Mark where platelets are.
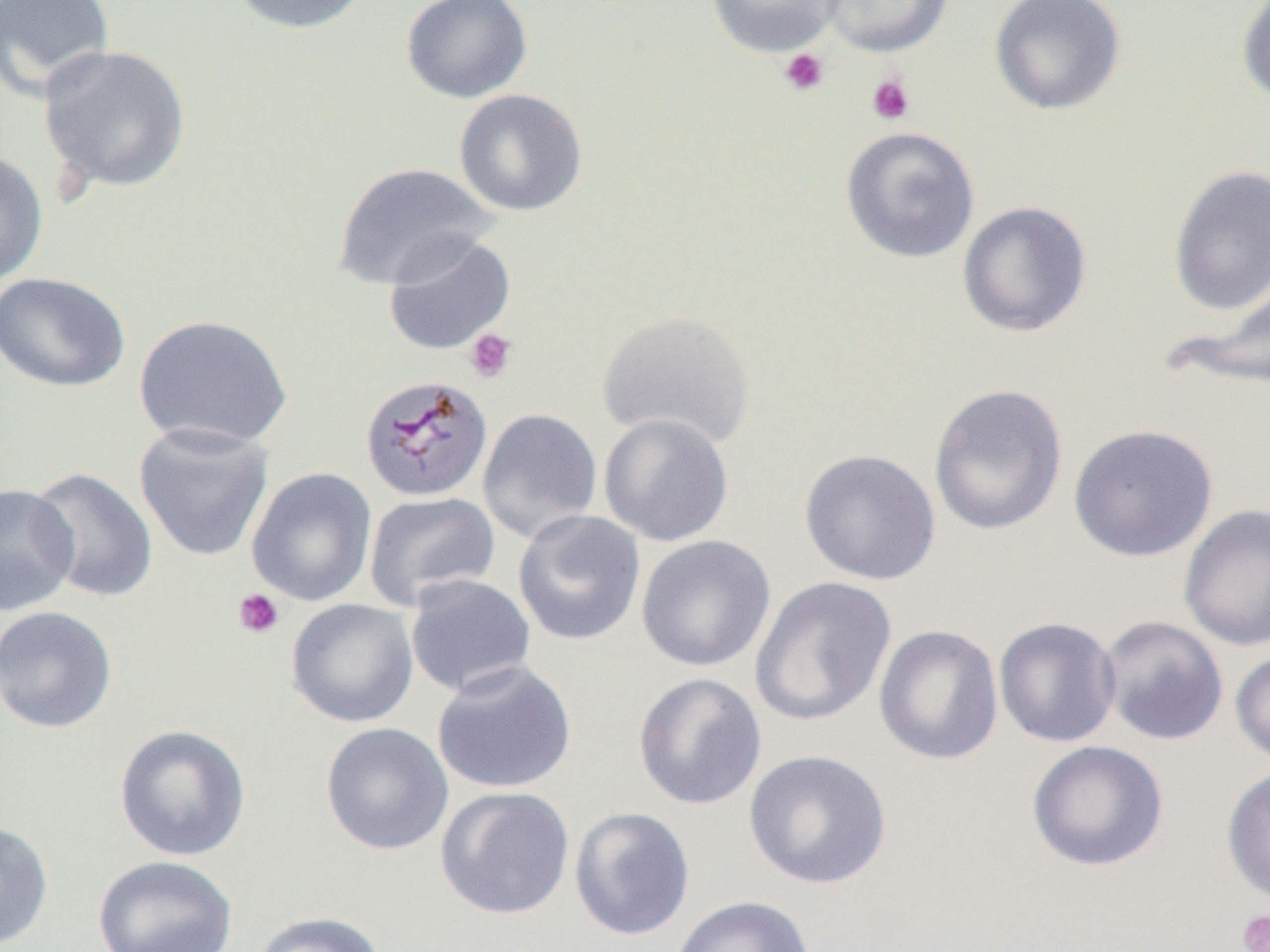

Approximate bounding boxes as (x1, y1, x2, y2) in pixels.
Platelets: (779, 48, 830, 96), (866, 74, 915, 125), (464, 328, 518, 383), (233, 588, 285, 639), (1237, 910, 1270, 952).

Summary:
  - Uninfected red blood cell locations: (0, 0, 116, 101), (226, 0, 373, 35), (399, 0, 533, 104), (705, 0, 845, 58), (819, 0, 954, 58), (988, 0, 1126, 116), (1236, 0, 1270, 106), (37, 44, 192, 195), (453, 88, 588, 217), (840, 125, 980, 264), (0, 149, 49, 287), (333, 162, 498, 289), (1167, 165, 1270, 315), (956, 200, 1092, 338), (382, 231, 516, 356), (0, 271, 131, 393), (1177, 273, 1269, 393), (597, 310, 755, 450), (133, 313, 293, 450), (927, 383, 1068, 537), (477, 407, 603, 544), (598, 413, 734, 546), (133, 422, 275, 562), (1068, 424, 1218, 562), (799, 448, 941, 585), (28, 467, 158, 604), (246, 467, 378, 606), (0, 484, 79, 616), (363, 490, 500, 611), (1178, 503, 1270, 652), (512, 510, 646, 645), (636, 535, 776, 672), (404, 574, 537, 698), (749, 577, 896, 728), (285, 598, 419, 728), (0, 605, 118, 733), (1098, 615, 1229, 746), (993, 616, 1121, 748), (874, 624, 1004, 765), (1230, 649, 1270, 769), (431, 660, 577, 794), (632, 672, 767, 810), (320, 722, 454, 856), (113, 723, 252, 862), (1027, 740, 1168, 872), (743, 749, 892, 890), (1221, 765, 1270, 907), (435, 786, 575, 920), (568, 805, 696, 941), (0, 820, 53, 949), (92, 855, 239, 952), (671, 895, 815, 952), (251, 911, 387, 952)
  - Plasmodium malariae-infected red blood cell locations: (359, 375, 493, 502)
  - Slide-level diagnosis: Plasmodium malariae
  - Magnification: 1000x
  - Field of view: single
  - Preparation: thin blood film
  - Modality: optical microscopy
  - Image size: 1270×952 pixels